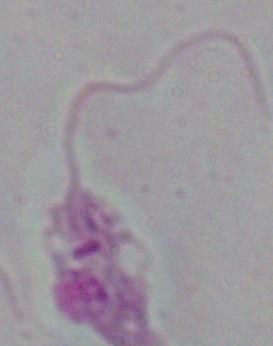

Summary:
  - Modality: photomicrograph
  - Magnification: 1000x
  - Identification: Leishmania